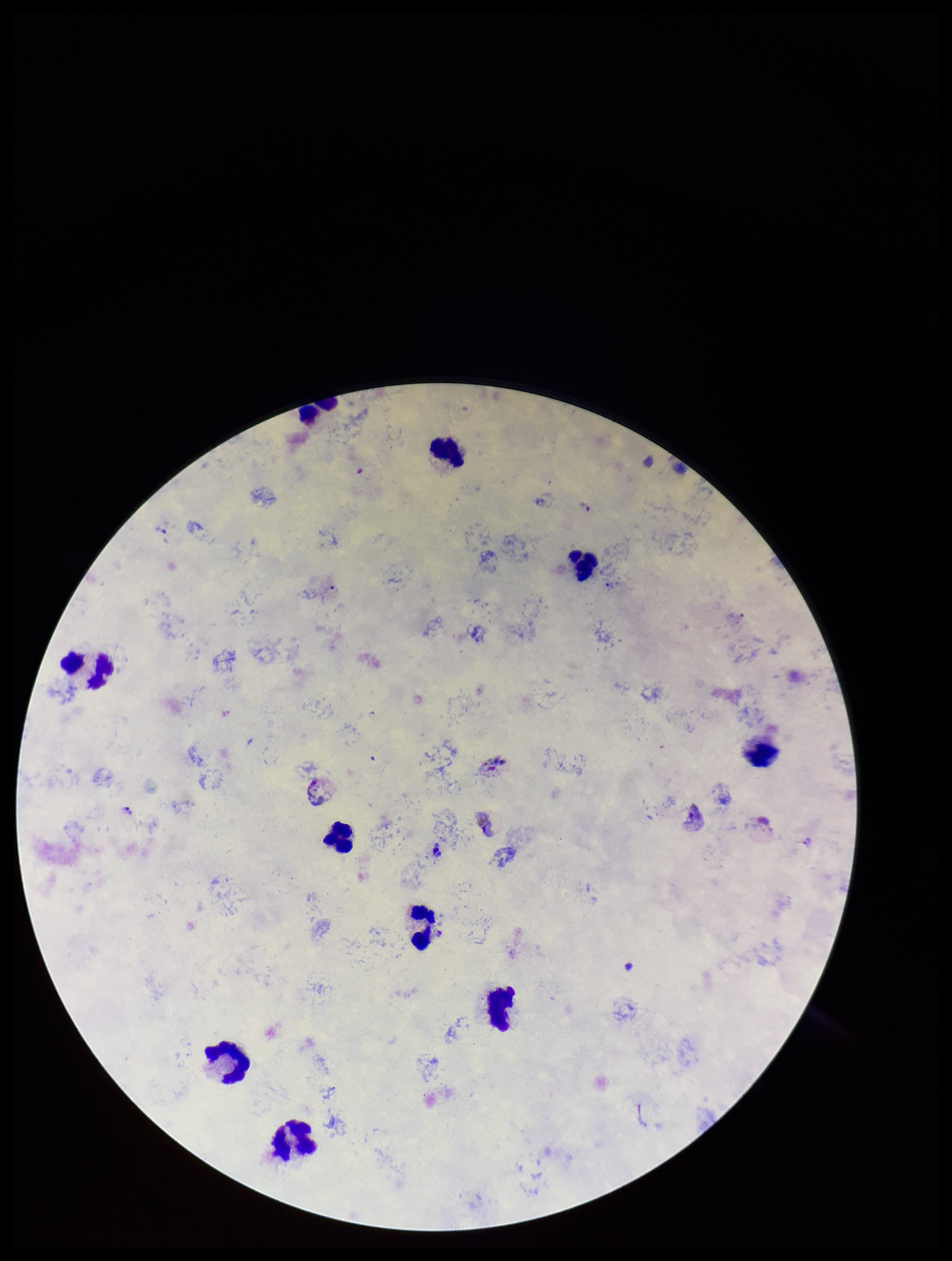

Summary:
  - Image size: 952×1261 pixels
  - Patient malaria status: positive
  - Field of view: single
  - Preparation: thick blood smear
  - Parasite count: 4
  - Species reported for this patient: Plasmodium vivax
  - Stain: Giemsa
  - Plasmodium parasites: identified
  - Leukocyte count: 11
  - Capture: smartphone photograph through the microscope eyepiece